Report the malaria status of this cell.
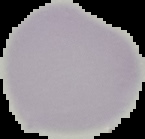
It is uninfected.

From a thin blood film. Image is 145×139 pixels. The area outside the segmented cell region is set to black.